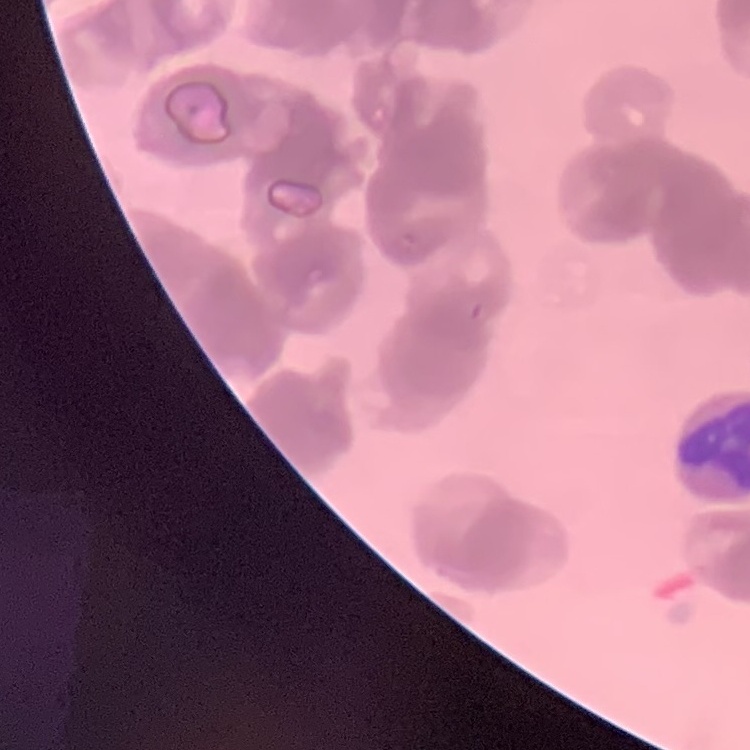
The erythrocytes show rouleaux formation. Thin blood film. One tile cut from a larger photomicrograph. Field's or Giemsa stain.